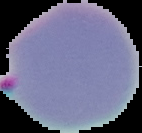
image_size: 142×133 pixels
result: Plasmodium parasites detected
image_type: cell region segmented out of the field of view; surrounding area masked to black
preparation: thin blood smear